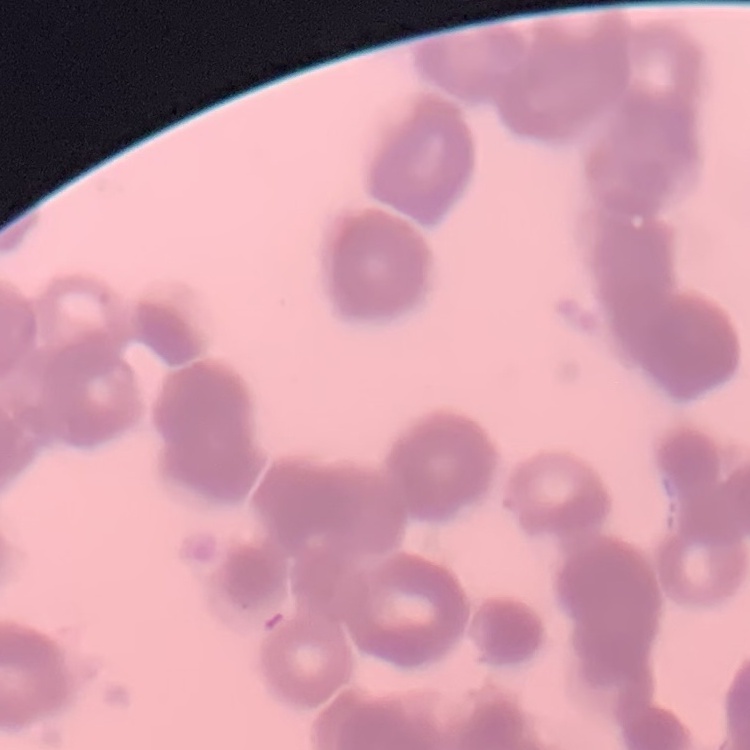

The red blood cells show rouleaux formation. Thin peripheral smear. Field's or Giemsa stain. Square crop of a larger photomicrograph.